Identify the cell.
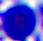

This is a leukocyte.

Micrograph. Captured at 400x magnification.